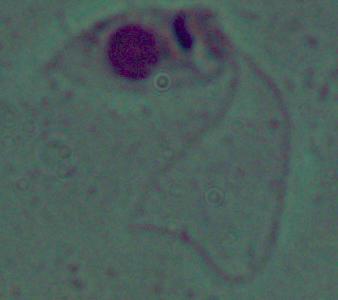 A Leishmania parasite is shown. Captured at 1000x magnification. Photomicrograph.